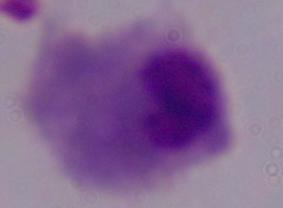

magnification = 1000x
identification = trichomonad
modality = photomicrograph